Assess this cell for malaria.
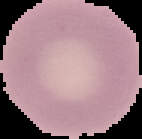
Uninfected.

Summary:
  - Image type: cell region segmented out of the field of view; surrounding area masked to black
  - Preparation: thin blood smear
  - Image size: 142×139 pixels